Assess this cell for malaria.
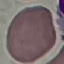
Uninfected.

Thin smear of blood. Automatically extracted cell patch, resized to 64 × 64 pixels. Giemsa stain. Photographed with a smartphone camera at the microscope eyepiece.